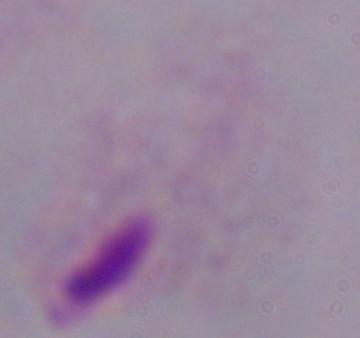
A trichomonad is shown. Photomicrograph. 1000x magnification.